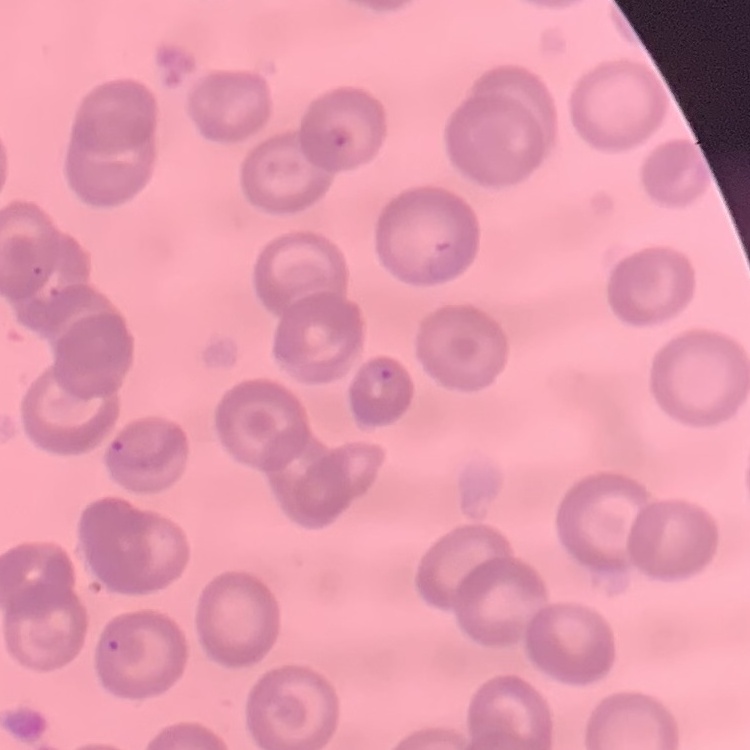 The red blood cells exhibit no rouleaux formation. Thin peripheral smear. Stained with either Field's or Giemsa. One tile cut from a larger photomicrograph.